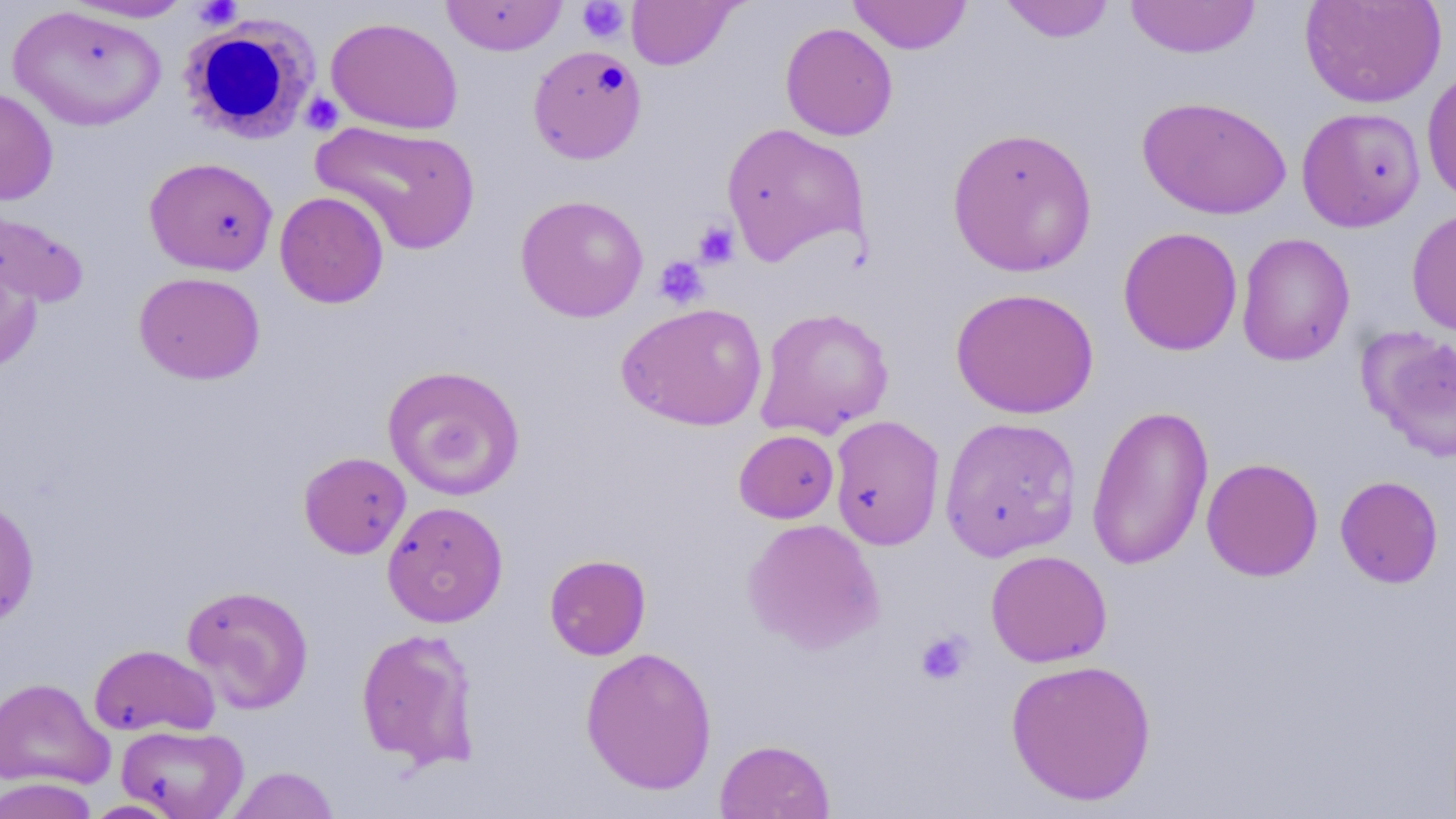

{
  "slide_level_diagnosis": "negative for blood parasites",
  "preparation": "thin blood smear",
  "image_size": "1456×819 pixels",
  "platelet_locations": "approximate bounding boxes as named x1/y1/x2/y2 corners in pixels: (x1=194, y1=0, x2=242, y2=31), (x1=576, y1=0, x2=630, y2=44), (x1=301, y1=92, x2=343, y2=134), (x1=692, y1=220, x2=740, y2=269), (x1=654, y1=256, x2=709, y2=309), (x1=916, y1=630, x2=973, y2=685)",
  "stain": "May-Grünwald-Giemsa",
  "modality": "light microscopy",
  "white_blood_cell_locations": "approximate bounding boxes as named x1/y1/x2/y2 corners in pixels: (x1=180, y1=17, x2=319, y2=144)",
  "uninfected_red_blood_cell_locations": "approximate bounding boxes as named x1/y1/x2/y2 corners in pixels: (x1=441, y1=0, x2=568, y2=56), (x1=626, y1=0, x2=739, y2=70), (x1=847, y1=0, x2=972, y2=54), (x1=1125, y1=0, x2=1261, y2=59), (x1=1299, y1=0, x2=1446, y2=108), (x1=61, y1=1, x2=197, y2=23), (x1=999, y1=1, x2=1117, y2=43), (x1=7, y1=4, x2=168, y2=132), (x1=325, y1=16, x2=464, y2=135), (x1=780, y1=22, x2=898, y2=141), (x1=528, y1=45, x2=647, y2=164), (x1=1421, y1=66, x2=1456, y2=206), (x1=0, y1=87, x2=59, y2=205), (x1=1136, y1=96, x2=1291, y2=219), (x1=1296, y1=106, x2=1426, y2=232), (x1=310, y1=119, x2=481, y2=255), (x1=720, y1=122, x2=870, y2=266), (x1=946, y1=126, x2=1098, y2=278), (x1=144, y1=156, x2=279, y2=276), (x1=274, y1=191, x2=389, y2=308), (x1=515, y1=194, x2=649, y2=323), (x1=0, y1=206, x2=90, y2=309), (x1=1406, y1=207, x2=1456, y2=338), (x1=1117, y1=226, x2=1243, y2=356), (x1=1236, y1=232, x2=1355, y2=366), (x1=0, y1=252, x2=43, y2=372), (x1=133, y1=271, x2=266, y2=385), (x1=949, y1=286, x2=1100, y2=419), (x1=617, y1=301, x2=768, y2=431), (x1=754, y1=306, x2=894, y2=439), (x1=1360, y1=326, x2=1456, y2=462), (x1=382, y1=364, x2=525, y2=500), (x1=1086, y1=403, x2=1213, y2=570), (x1=828, y1=415, x2=946, y2=551), (x1=939, y1=416, x2=1082, y2=561), (x1=734, y1=429, x2=839, y2=523), (x1=298, y1=451, x2=411, y2=559), (x1=1201, y1=457, x2=1324, y2=581), (x1=1334, y1=475, x2=1444, y2=588), (x1=0, y1=496, x2=40, y2=628), (x1=382, y1=501, x2=509, y2=627), (x1=743, y1=517, x2=885, y2=654), (x1=985, y1=550, x2=1112, y2=668), (x1=544, y1=554, x2=651, y2=660), (x1=181, y1=584, x2=314, y2=714), (x1=356, y1=627, x2=480, y2=770), (x1=88, y1=644, x2=220, y2=738), (x1=580, y1=646, x2=718, y2=796), (x1=1004, y1=658, x2=1157, y2=806), (x1=0, y1=676, x2=114, y2=790), (x1=117, y1=724, x2=249, y2=819), (x1=714, y1=739, x2=835, y2=819), (x1=226, y1=765, x2=340, y2=819), (x1=0, y1=777, x2=99, y2=819), (x1=83, y1=799, x2=184, y2=818)",
  "field_of_view": "one of a larger specimen",
  "magnification": "1000x"
}